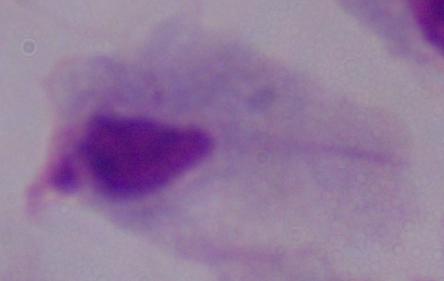
Summary:
  - Identification: trichomonad
  - Magnification: 1000x
  - Modality: micrograph